Outline each Plasmodium falciparum-infected red blood cell.
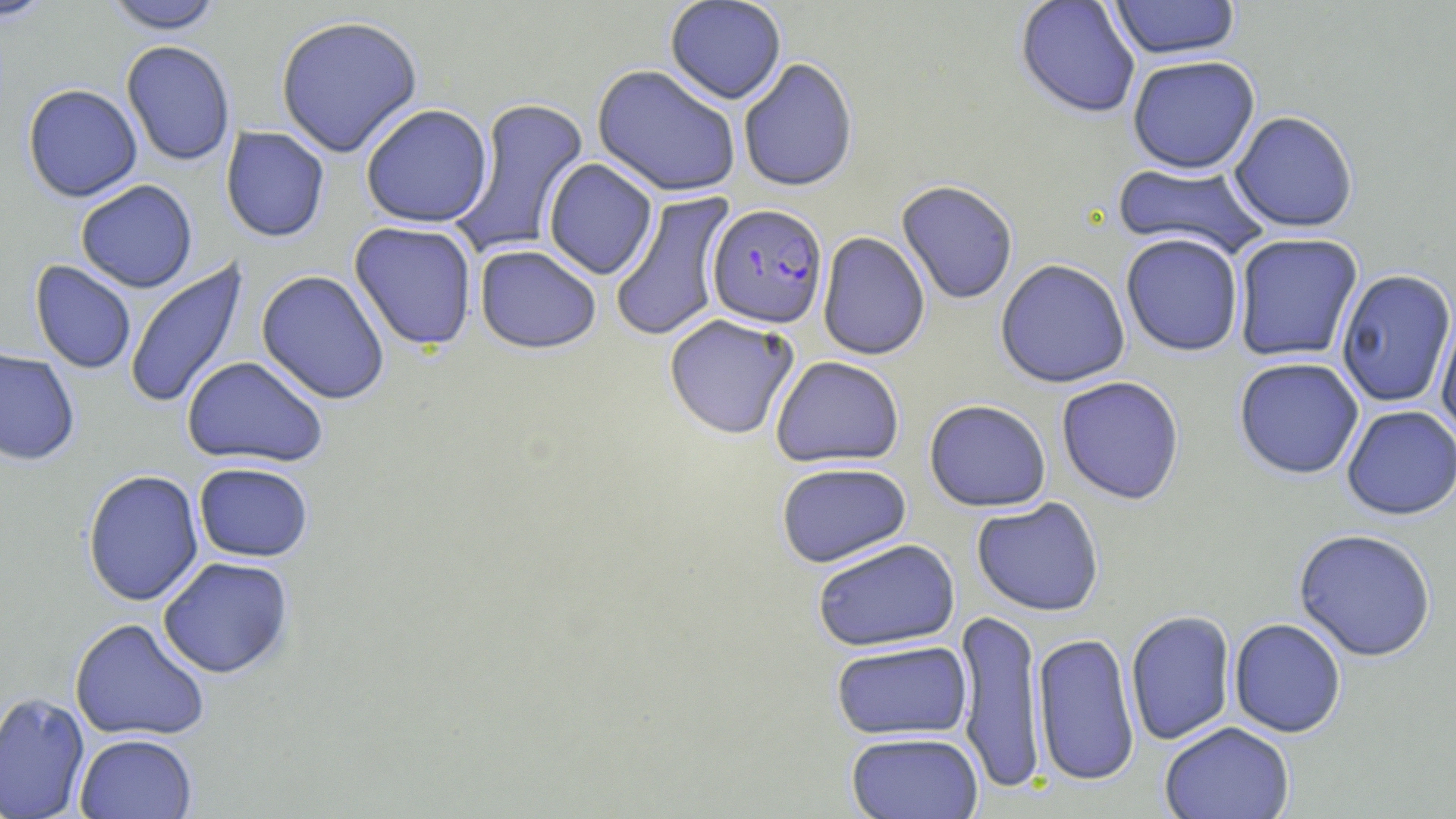
Approximate bounding boxes as (x1,y1)-(x2,y2) corner pairs in pixels.
Plasmodium falciparum-infected red blood cells: (707,203)-(828,330).

{
  "slide_level_diagnosis": "Plasmodium falciparum",
  "stain": "May-Grünwald-Giemsa",
  "field_of_view": "one of a larger specimen",
  "uninfected_red_blood_cell_locations": "approximate bounding boxes as (x1,y1)-(x2,y2) corner pairs in pixels: (0,0)-(60,24), (664,0)-(787,105), (1015,0)-(1141,120), (1109,0)-(1241,62), (103,1)-(224,34), (274,14)-(424,158), (121,40)-(236,167), (1127,56)-(1261,176), (738,58)-(859,194), (592,65)-(742,198), (22,84)-(143,202), (450,97)-(591,259), (360,104)-(493,228), (1228,112)-(1358,234), (220,126)-(331,243), (543,158)-(658,280), (1111,161)-(1270,260), (75,180)-(198,293), (896,180)-(1018,305), (609,190)-(735,343), (349,221)-(478,350), (817,232)-(930,360), (1120,234)-(1244,357), (1232,234)-(1364,363), (474,244)-(602,355), (124,257)-(251,411), (995,259)-(1131,388), (29,260)-(137,374), (256,269)-(391,405), (1335,270)-(1456,408), (1434,308)-(1456,444), (663,313)-(800,440), (0,346)-(81,466), (181,355)-(330,469), (770,356)-(905,468), (1233,357)-(1364,480), (1056,376)-(1185,505), (923,399)-(1052,512), (1341,405)-(1456,521), (193,462)-(314,562), (775,462)-(912,568), (82,470)-(204,606), (970,497)-(1105,617), (1293,529)-(1437,662), (812,538)-(961,652), (157,556)-(294,679), (955,607)-(1046,795), (1125,610)-(1236,746), (70,617)-(211,742), (1229,618)-(1347,738), (1032,632)-(1140,787), (830,640)-(973,740), (0,691)-(90,819), (1159,722)-(1295,819), (845,731)-(984,819), (74,733)-(198,819)",
  "image_size": "1456×819 pixels",
  "modality": "light microscopy",
  "preparation": "thin blood smear",
  "magnification": "1000x"
}